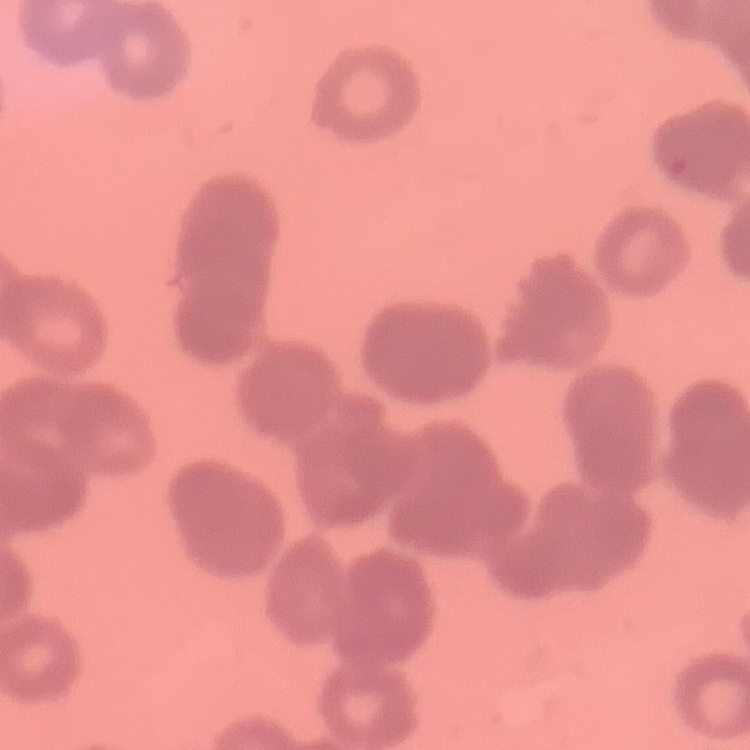

Summary:
  - Erythrocyte morphology: rouleaux formation
  - Stain: Field's or Giemsa
  - Image type: one tile cut from a larger photomicrograph
  - Preparation: thin peripheral smear